Identify the blood parasite species.
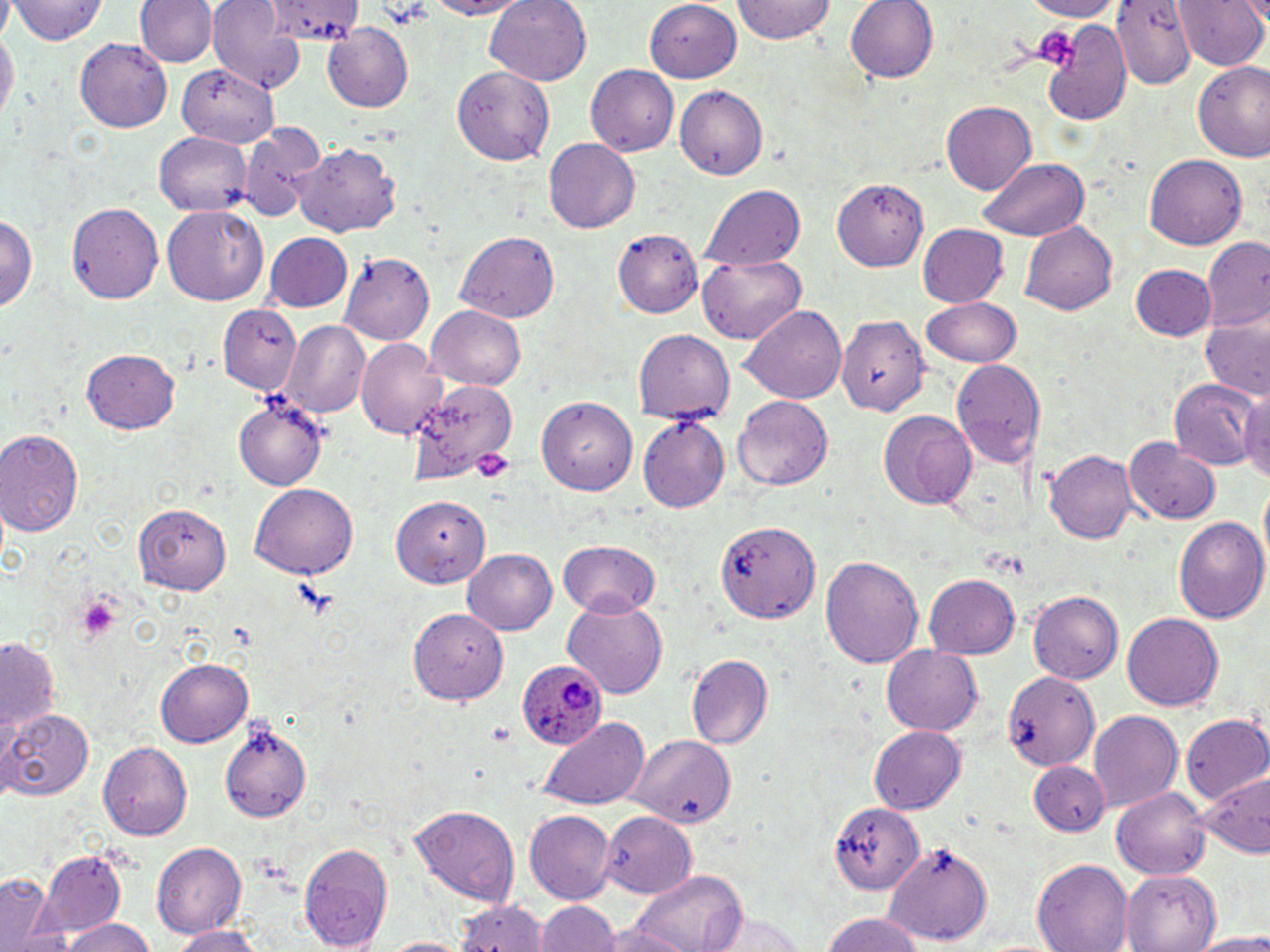

Plasmodium ovale.

Summary:
  - Coordinate format: approximate bounding boxes as named x1/y1/x2/y2 corners in pixels
  - Platelet locations: (x1=379, y1=0, x2=434, y2=28), (x1=1030, y1=22, x2=1082, y2=70), (x1=471, y1=446, x2=515, y2=482), (x1=69, y1=593, x2=123, y2=646), (x1=487, y1=723, x2=515, y2=745)
  - Uninfected red blood cell locations: (x1=10, y1=0, x2=108, y2=47), (x1=136, y1=0, x2=215, y2=68), (x1=210, y1=0, x2=311, y2=91), (x1=271, y1=0, x2=366, y2=41), (x1=417, y1=0, x2=543, y2=20), (x1=483, y1=0, x2=593, y2=87), (x1=734, y1=0, x2=836, y2=45), (x1=846, y1=0, x2=939, y2=84), (x1=1013, y1=0, x2=1129, y2=20), (x1=1114, y1=0, x2=1194, y2=84), (x1=1173, y1=0, x2=1267, y2=72), (x1=644, y1=2, x2=741, y2=84), (x1=1042, y1=16, x2=1133, y2=128), (x1=0, y1=23, x2=16, y2=130), (x1=324, y1=26, x2=414, y2=110), (x1=73, y1=37, x2=172, y2=134), (x1=1192, y1=61, x2=1270, y2=159), (x1=177, y1=62, x2=280, y2=144), (x1=454, y1=65, x2=555, y2=165), (x1=586, y1=66, x2=678, y2=157), (x1=676, y1=84, x2=768, y2=180), (x1=941, y1=100, x2=1039, y2=195), (x1=237, y1=122, x2=327, y2=221), (x1=153, y1=131, x2=250, y2=213), (x1=545, y1=139, x2=640, y2=232), (x1=291, y1=142, x2=403, y2=240), (x1=1147, y1=154, x2=1245, y2=251), (x1=979, y1=158, x2=1092, y2=241), (x1=833, y1=176, x2=929, y2=270), (x1=705, y1=185, x2=806, y2=270), (x1=67, y1=202, x2=165, y2=305), (x1=162, y1=206, x2=269, y2=307), (x1=1, y1=210, x2=39, y2=316), (x1=1021, y1=220, x2=1119, y2=316), (x1=915, y1=224, x2=1007, y2=308), (x1=615, y1=229, x2=703, y2=318), (x1=264, y1=231, x2=355, y2=313), (x1=454, y1=231, x2=561, y2=322), (x1=1202, y1=238, x2=1270, y2=329), (x1=341, y1=252, x2=433, y2=343), (x1=698, y1=255, x2=804, y2=341), (x1=1131, y1=265, x2=1216, y2=341), (x1=921, y1=297, x2=1021, y2=367), (x1=218, y1=303, x2=301, y2=395), (x1=426, y1=304, x2=529, y2=394), (x1=740, y1=305, x2=850, y2=405), (x1=836, y1=311, x2=928, y2=414), (x1=1200, y1=314, x2=1269, y2=403), (x1=281, y1=323, x2=369, y2=418), (x1=634, y1=329, x2=735, y2=425), (x1=357, y1=339, x2=449, y2=439), (x1=83, y1=349, x2=181, y2=435), (x1=950, y1=361, x2=1044, y2=470), (x1=1168, y1=376, x2=1259, y2=467), (x1=408, y1=382, x2=513, y2=478), (x1=1237, y1=384, x2=1270, y2=489), (x1=539, y1=396, x2=638, y2=495), (x1=733, y1=396, x2=834, y2=491), (x1=235, y1=397, x2=327, y2=489), (x1=877, y1=411, x2=976, y2=509), (x1=638, y1=417, x2=729, y2=511), (x1=0, y1=430, x2=84, y2=539), (x1=1125, y1=435, x2=1220, y2=522), (x1=1044, y1=447, x2=1135, y2=546), (x1=249, y1=482, x2=359, y2=579), (x1=392, y1=493, x2=489, y2=587), (x1=137, y1=504, x2=232, y2=594), (x1=1173, y1=514, x2=1268, y2=624), (x1=715, y1=517, x2=822, y2=625), (x1=558, y1=540, x2=662, y2=618), (x1=462, y1=547, x2=558, y2=634), (x1=822, y1=554, x2=922, y2=670), (x1=924, y1=575, x2=1019, y2=659), (x1=1027, y1=590, x2=1123, y2=684), (x1=561, y1=600, x2=667, y2=698), (x1=407, y1=608, x2=504, y2=705), (x1=1121, y1=613, x2=1223, y2=712), (x1=0, y1=638, x2=59, y2=740), (x1=882, y1=646, x2=983, y2=735), (x1=684, y1=651, x2=773, y2=752), (x1=155, y1=660, x2=251, y2=747), (x1=998, y1=665, x2=1098, y2=774), (x1=1, y1=707, x2=93, y2=801), (x1=1090, y1=711, x2=1182, y2=810), (x1=1181, y1=713, x2=1270, y2=806), (x1=534, y1=714, x2=654, y2=809), (x1=218, y1=717, x2=312, y2=825), (x1=868, y1=725, x2=967, y2=815), (x1=625, y1=736, x2=737, y2=826), (x1=97, y1=740, x2=192, y2=840), (x1=1026, y1=760, x2=1109, y2=838), (x1=1196, y1=773, x2=1268, y2=856), (x1=1114, y1=787, x2=1212, y2=878), (x1=829, y1=799, x2=924, y2=894), (x1=409, y1=807, x2=519, y2=903), (x1=522, y1=808, x2=615, y2=903), (x1=600, y1=809, x2=695, y2=896), (x1=298, y1=840, x2=393, y2=950), (x1=153, y1=841, x2=247, y2=940), (x1=885, y1=843, x2=993, y2=944), (x1=40, y1=851, x2=128, y2=933), (x1=1031, y1=859, x2=1133, y2=952), (x1=1123, y1=867, x2=1220, y2=950), (x1=631, y1=870, x2=745, y2=952), (x1=0, y1=875, x2=67, y2=952), (x1=455, y1=896, x2=547, y2=952), (x1=536, y1=899, x2=620, y2=952), (x1=706, y1=908, x2=811, y2=952), (x1=820, y1=913, x2=925, y2=952), (x1=59, y1=916, x2=155, y2=952), (x1=590, y1=922, x2=696, y2=952), (x1=165, y1=925, x2=266, y2=952), (x1=1189, y1=932, x2=1270, y2=952), (x1=377, y1=936, x2=475, y2=952)
  - Plasmodium ovale-infected red blood cell locations: (x1=519, y1=658, x2=607, y2=750)
  - Field of view: one of a larger specimen
  - Image size: 1270×952 pixels
  - Modality: optical microscopy
  - Magnification: 1000x
  - Stain: May-Grünwald-Giemsa
  - Preparation: thin blood smear